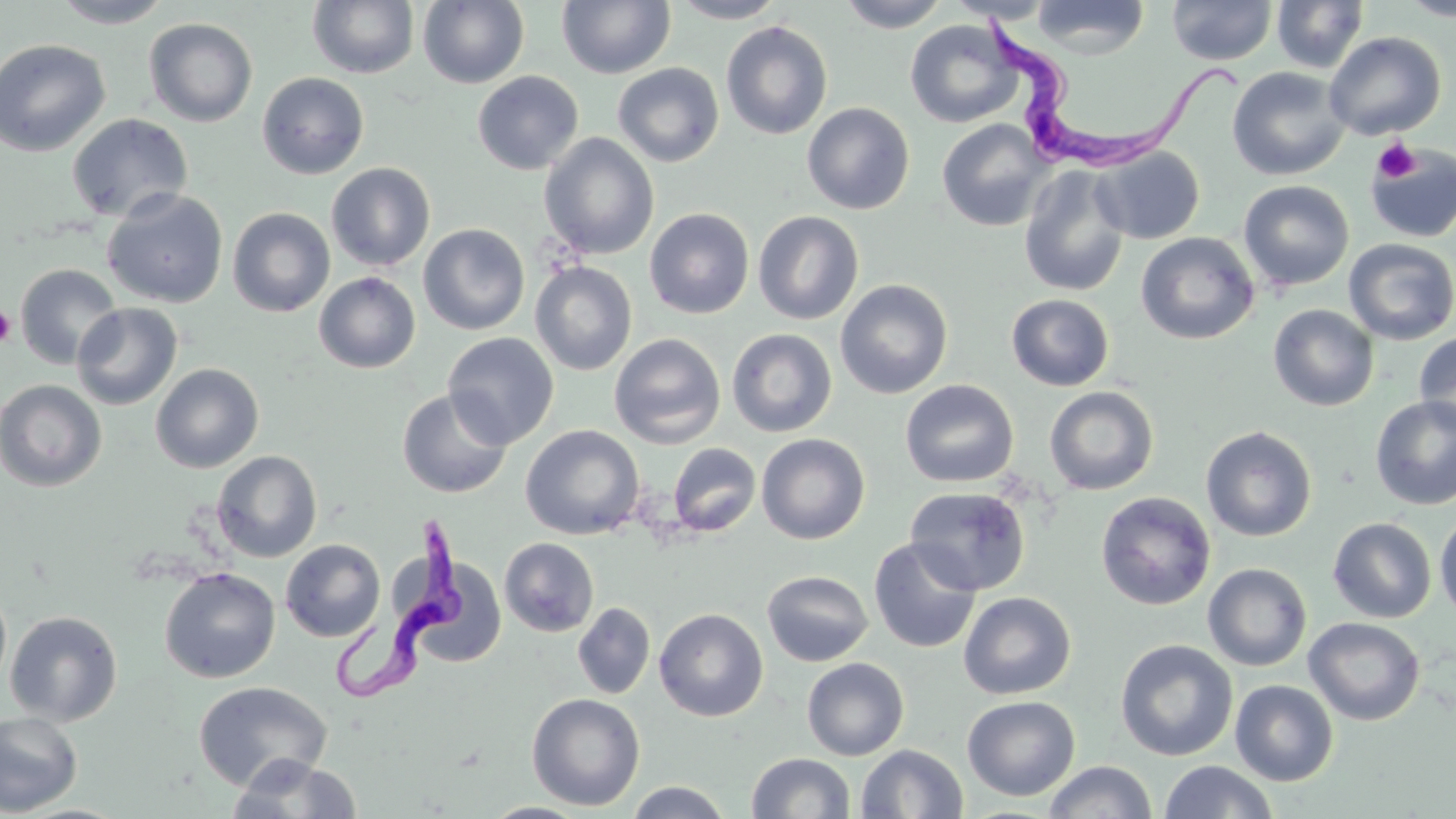

Summary:
  - Coordinate format: approximate bounding boxes as (x1,y1)-(x2,y2) corner pairs in pixels
  - Platelet locations: (1372,138)-(1420,183), (1,304)-(16,348)
  - Trypanosoma brucei locations: (981,19)-(1249,163), (324,514)-(472,706)
  - Uninfected red blood cell locations: (49,0)-(175,28), (668,0)-(790,23), (836,0)-(951,32), (945,0)-(1058,23), (1030,0)-(1149,58), (1167,0)-(1278,66), (1271,0)-(1369,74), (1397,0)-(1456,21), (308,1)-(420,79), (419,1)-(529,89), (557,1)-(676,79), (144,18)-(258,127), (905,20)-(1023,128), (721,21)-(833,140), (1323,31)-(1446,141), (0,39)-(111,157), (612,62)-(725,167), (1227,66)-(1351,181), (472,71)-(583,175), (257,72)-(369,179), (802,101)-(915,215), (67,113)-(193,223), (936,119)-(1053,231), (539,133)-(659,260), (1365,143)-(1456,243), (1091,146)-(1205,244), (326,162)-(435,271), (1019,166)-(1130,296), (1238,180)-(1354,291), (102,189)-(228,308), (227,207)-(335,317), (645,208)-(754,319), (752,210)-(864,325), (418,223)-(530,335), (1136,233)-(1259,344), (1343,238)-(1456,345), (531,261)-(637,375), (15,263)-(122,370), (313,271)-(421,373), (835,278)-(954,399), (1006,294)-(1114,391), (72,302)-(182,410), (1267,304)-(1379,411), (726,328)-(837,437), (1413,331)-(1456,434), (442,332)-(559,448), (609,333)-(726,449), (150,364)-(264,473), (0,379)-(107,492), (900,379)-(1018,488), (1044,386)-(1159,495), (397,388)-(513,498), (1370,395)-(1456,510), (521,424)-(645,539), (1201,425)-(1317,542), (756,433)-(870,544), (668,442)-(761,537), (211,451)-(322,562), (904,485)-(1031,596), (1096,491)-(1216,611), (1435,511)-(1456,623), (1328,517)-(1436,623), (499,537)-(599,637), (868,537)-(982,653), (280,539)-(385,642), (413,558)-(507,668), (1203,563)-(1312,671), (159,567)-(280,684), (762,570)-(873,667), (0,585)-(12,692), (959,591)-(1076,699), (572,602)-(656,699), (654,608)-(768,721), (5,610)-(123,726), (1303,617)-(1425,725), (1114,639)-(1238,762), (801,657)-(909,760), (1230,679)-(1339,785), (193,681)-(332,791), (526,692)-(646,811), (962,695)-(1080,801), (0,711)-(83,817), (855,744)-(968,818), (746,752)-(856,818), (228,755)-(363,818), (1043,760)-(1158,818), (1158,761)-(1279,819), (624,781)-(734,818), (480,802)-(590,819)
  - Slide-level diagnosis: Trypanosoma brucei
  - Modality: light microscopy
  - Magnification: 1000x
  - Stain: May-Grünwald-Giemsa
  - Field of view: single
  - Image size: 1456×819 pixels
  - Preparation: thin blood smear